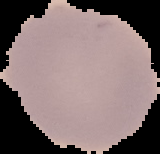
{
  "malaria_status": "uninfected",
  "image_type": "cell region segmented out of the field of view; surrounding area masked to black",
  "image_size": "160×154 pixels",
  "preparation": "thin blood smear"
}